Name the blood parasite species.
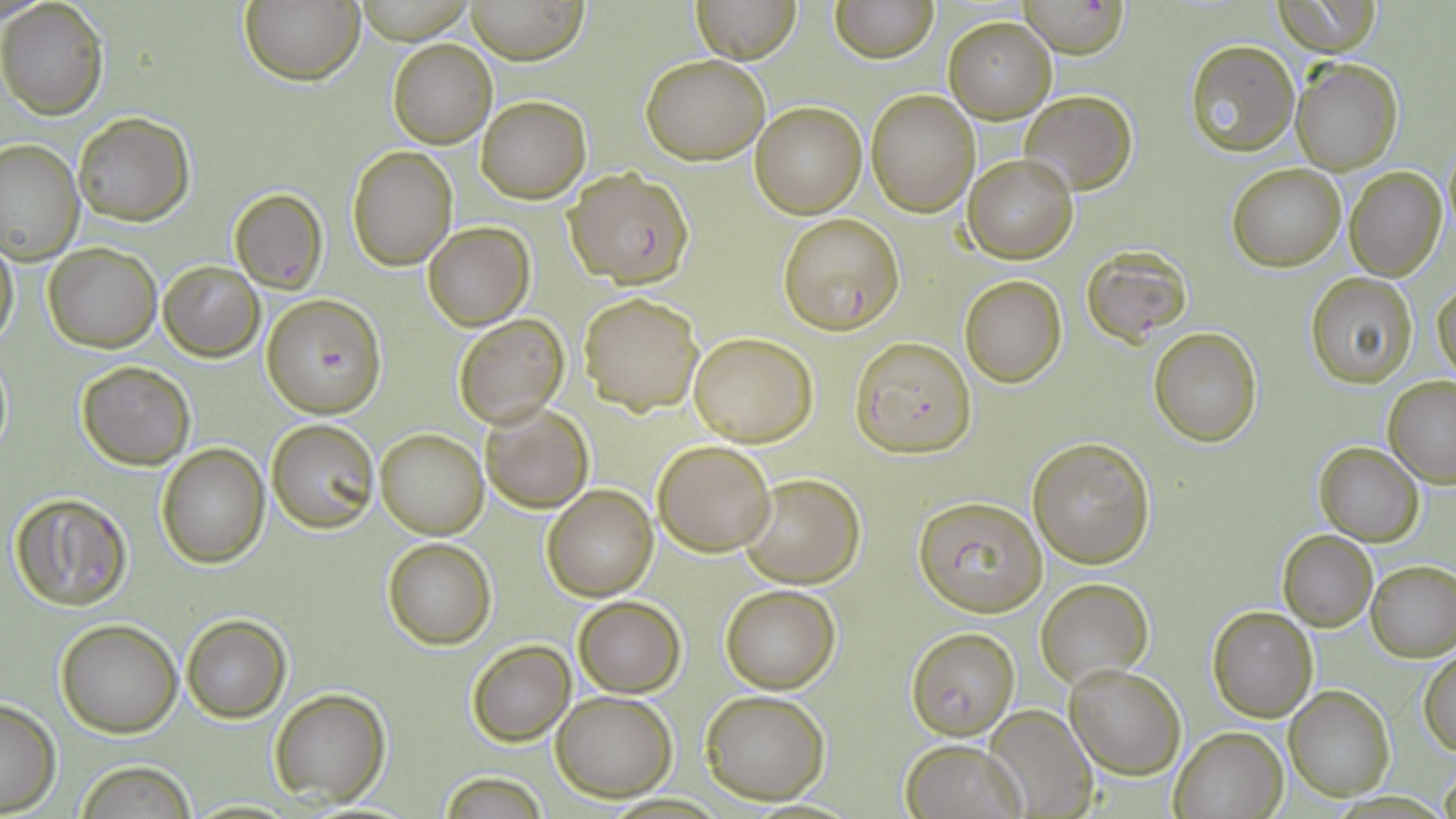
Plasmodium falciparum.

Approximate bounding boxes as (x1, y1, x2, y2) in pixels. Uninfected red blood cell locations: (240, 0, 365, 85), (466, 0, 589, 63), (693, 0, 800, 62), (830, 0, 938, 64), (1271, 0, 1384, 55), (0, 1, 109, 119), (944, 17, 1056, 122), (387, 38, 497, 148), (1184, 39, 1300, 155), (642, 55, 767, 163), (1290, 57, 1403, 174), (866, 90, 979, 217), (1020, 90, 1136, 194), (476, 96, 591, 204), (750, 101, 866, 218), (73, 112, 195, 225), (0, 141, 82, 262), (1442, 143, 1456, 242), (347, 147, 458, 270), (964, 155, 1077, 263), (1227, 163, 1346, 271), (1345, 167, 1445, 280), (229, 188, 328, 293), (423, 222, 533, 330), (0, 231, 19, 352), (43, 242, 162, 351), (158, 261, 263, 362), (1306, 273, 1417, 386), (959, 276, 1066, 387), (1432, 279, 1456, 386), (578, 291, 703, 415), (452, 313, 569, 428), (1149, 326, 1262, 446), (687, 331, 818, 446), (1, 349, 13, 464), (76, 360, 195, 470), (1383, 375, 1456, 488), (480, 403, 594, 513), (266, 418, 379, 532), (374, 428, 488, 539), (1027, 437, 1155, 568), (653, 440, 777, 554), (1314, 442, 1424, 545), (157, 444, 268, 567), (738, 471, 863, 588), (542, 486, 658, 600), (1277, 530, 1377, 630), (381, 537, 497, 649), (1366, 561, 1456, 661), (1035, 576, 1154, 690), (720, 583, 842, 693), (571, 595, 686, 697), (1206, 605, 1319, 723), (181, 614, 290, 722), (55, 618, 182, 736), (466, 641, 574, 747), (1419, 653, 1456, 754), (1064, 665, 1186, 780), (1285, 686, 1394, 800), (269, 687, 391, 807), (551, 689, 678, 801), (700, 689, 832, 804), (0, 696, 62, 815), (987, 704, 1096, 816), (1168, 725, 1288, 818), (902, 740, 1026, 819), (72, 762, 198, 818), (1440, 764, 1456, 819), (438, 774, 552, 816). Plasmodium falciparum-infected red blood cell locations: (1018, 0, 1130, 58), (567, 167, 694, 287), (777, 212, 904, 334), (1082, 248, 1191, 347), (261, 295, 387, 418), (851, 336, 975, 458), (8, 491, 134, 611), (912, 493, 1046, 619), (906, 628, 1020, 739). Single field of view. May-Grünwald-Giemsa-stained preparation. Captured at 1000x magnification. Thin blood smear. Optical microscopy. Image is 1456×819 pixels.